Locate and identify every blood parasite.
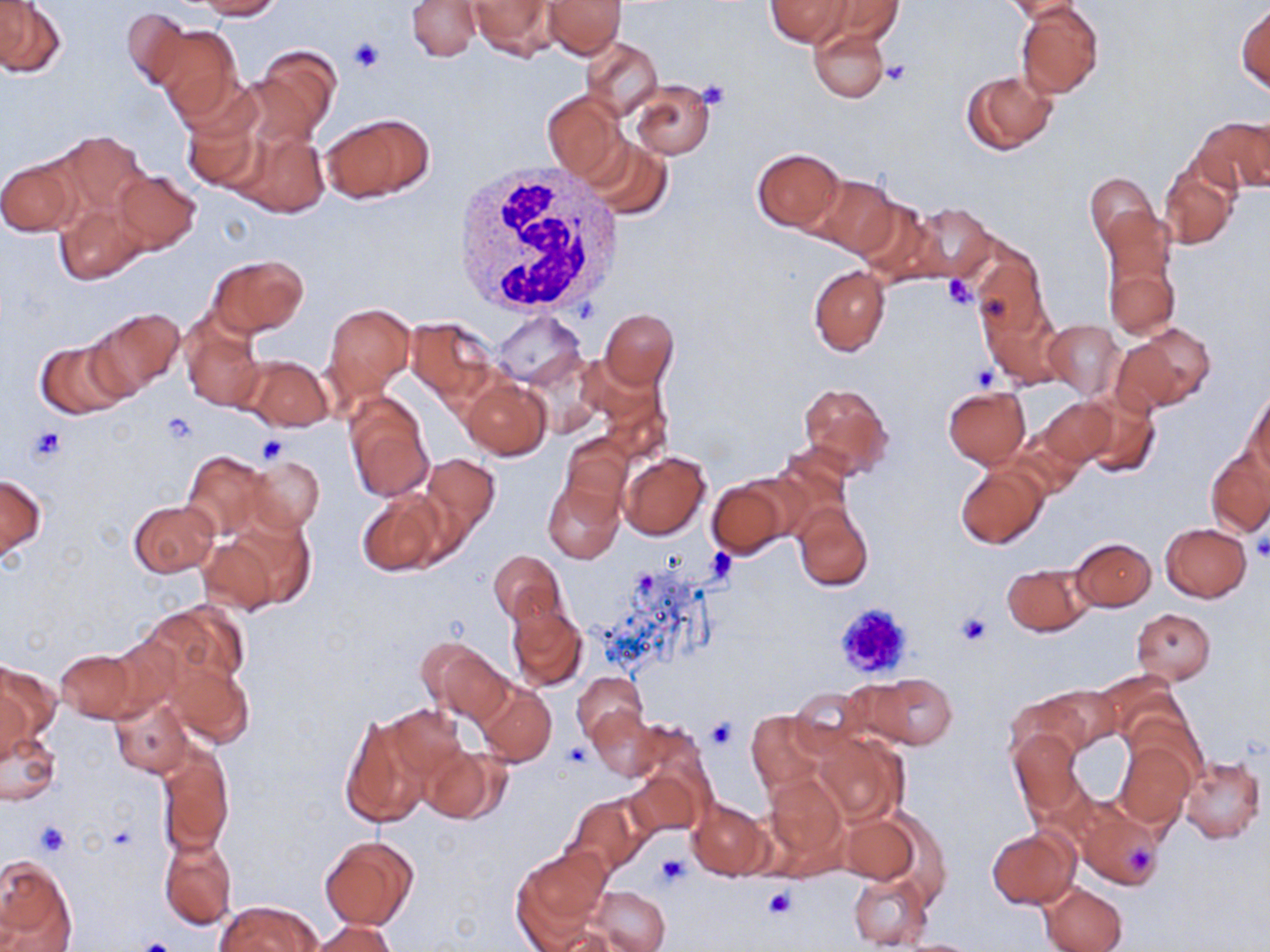
No blood parasites observed.

Summary:
  - Coordinate format: approximate bounding boxes as named x1/y1/x2/y2 corners in pixels
  - Platelet locations: (x1=348, y1=38, x2=383, y2=74), (x1=882, y1=61, x2=911, y2=86), (x1=695, y1=79, x2=731, y2=111), (x1=941, y1=277, x2=979, y2=311), (x1=973, y1=364, x2=1001, y2=390), (x1=160, y1=413, x2=198, y2=446), (x1=25, y1=425, x2=66, y2=464), (x1=258, y1=434, x2=290, y2=464), (x1=1251, y1=537, x2=1270, y2=563), (x1=831, y1=601, x2=915, y2=680), (x1=955, y1=613, x2=990, y2=647), (x1=705, y1=719, x2=737, y2=749), (x1=562, y1=743, x2=591, y2=770), (x1=35, y1=821, x2=68, y2=856), (x1=655, y1=852, x2=688, y2=886), (x1=763, y1=885, x2=797, y2=920), (x1=134, y1=936, x2=178, y2=952)
  - Uninfected red blood cell locations: (x1=198, y1=0, x2=280, y2=19), (x1=407, y1=0, x2=480, y2=61), (x1=543, y1=0, x2=624, y2=57), (x1=819, y1=0, x2=903, y2=45), (x1=466, y1=1, x2=559, y2=60), (x1=766, y1=1, x2=854, y2=47), (x1=1003, y1=1, x2=1084, y2=21), (x1=0, y1=2, x2=64, y2=76), (x1=1015, y1=2, x2=1104, y2=98), (x1=1237, y1=5, x2=1270, y2=94), (x1=122, y1=6, x2=189, y2=91), (x1=152, y1=23, x2=244, y2=122), (x1=809, y1=25, x2=891, y2=103), (x1=583, y1=38, x2=661, y2=117), (x1=250, y1=46, x2=342, y2=143), (x1=962, y1=70, x2=1056, y2=155), (x1=631, y1=81, x2=714, y2=159), (x1=542, y1=91, x2=625, y2=179), (x1=181, y1=107, x2=266, y2=193), (x1=320, y1=113, x2=436, y2=204), (x1=1194, y1=116, x2=1270, y2=195), (x1=233, y1=128, x2=330, y2=218), (x1=53, y1=130, x2=151, y2=221), (x1=583, y1=138, x2=673, y2=220), (x1=752, y1=148, x2=845, y2=232), (x1=0, y1=156, x2=79, y2=237), (x1=1158, y1=161, x2=1238, y2=248), (x1=112, y1=171, x2=201, y2=254), (x1=1085, y1=172, x2=1158, y2=252), (x1=804, y1=175, x2=900, y2=259), (x1=852, y1=199, x2=944, y2=285), (x1=55, y1=201, x2=149, y2=285), (x1=907, y1=203, x2=995, y2=283), (x1=1102, y1=229, x2=1179, y2=340), (x1=970, y1=247, x2=1047, y2=337), (x1=207, y1=253, x2=309, y2=337), (x1=808, y1=266, x2=890, y2=356), (x1=980, y1=301, x2=1065, y2=389), (x1=323, y1=302, x2=415, y2=401), (x1=83, y1=307, x2=185, y2=399), (x1=600, y1=309, x2=678, y2=389), (x1=490, y1=310, x2=588, y2=387), (x1=181, y1=315, x2=263, y2=412), (x1=404, y1=317, x2=500, y2=406), (x1=1043, y1=319, x2=1124, y2=401), (x1=1116, y1=323, x2=1210, y2=413), (x1=35, y1=340, x2=131, y2=421), (x1=239, y1=354, x2=332, y2=431), (x1=462, y1=378, x2=551, y2=460), (x1=797, y1=381, x2=893, y2=479), (x1=944, y1=386, x2=1030, y2=467), (x1=1244, y1=388, x2=1270, y2=480), (x1=344, y1=392, x2=433, y2=502), (x1=1075, y1=394, x2=1160, y2=478), (x1=1038, y1=399, x2=1115, y2=466), (x1=559, y1=433, x2=633, y2=515), (x1=1207, y1=449, x2=1270, y2=537), (x1=182, y1=450, x2=268, y2=540), (x1=619, y1=451, x2=710, y2=540), (x1=420, y1=454, x2=501, y2=542), (x1=248, y1=457, x2=324, y2=532), (x1=956, y1=465, x2=1048, y2=549), (x1=0, y1=474, x2=46, y2=559), (x1=541, y1=478, x2=625, y2=565), (x1=707, y1=479, x2=793, y2=557), (x1=355, y1=489, x2=447, y2=578), (x1=129, y1=500, x2=219, y2=577), (x1=793, y1=501, x2=873, y2=591), (x1=1160, y1=523, x2=1253, y2=602), (x1=196, y1=534, x2=283, y2=615), (x1=1071, y1=536, x2=1156, y2=610), (x1=488, y1=548, x2=566, y2=629), (x1=1002, y1=564, x2=1091, y2=637), (x1=147, y1=600, x2=251, y2=691), (x1=507, y1=600, x2=589, y2=692), (x1=1132, y1=608, x2=1216, y2=683), (x1=420, y1=637, x2=511, y2=725), (x1=56, y1=649, x2=139, y2=722), (x1=166, y1=661, x2=253, y2=746), (x1=0, y1=662, x2=59, y2=752), (x1=572, y1=672, x2=646, y2=742), (x1=863, y1=673, x2=957, y2=749), (x1=475, y1=681, x2=556, y2=766), (x1=1046, y1=684, x2=1123, y2=753), (x1=788, y1=688, x2=868, y2=755), (x1=1008, y1=694, x2=1088, y2=764), (x1=109, y1=695, x2=192, y2=778), (x1=383, y1=704, x2=468, y2=783), (x1=589, y1=707, x2=662, y2=780), (x1=747, y1=711, x2=826, y2=793), (x1=338, y1=714, x2=430, y2=828), (x1=628, y1=722, x2=711, y2=808), (x1=1, y1=725, x2=61, y2=807), (x1=1008, y1=729, x2=1086, y2=817), (x1=815, y1=732, x2=907, y2=826), (x1=1114, y1=740, x2=1194, y2=829), (x1=157, y1=743, x2=233, y2=855), (x1=420, y1=744, x2=509, y2=824), (x1=1177, y1=756, x2=1265, y2=843), (x1=623, y1=765, x2=706, y2=839), (x1=764, y1=773, x2=846, y2=871), (x1=567, y1=794, x2=650, y2=876), (x1=687, y1=796, x2=770, y2=881), (x1=1066, y1=796, x2=1166, y2=890), (x1=840, y1=814, x2=918, y2=884), (x1=988, y1=828, x2=1080, y2=909), (x1=159, y1=836, x2=237, y2=929), (x1=320, y1=836, x2=417, y2=929), (x1=514, y1=845, x2=611, y2=943), (x1=0, y1=854, x2=75, y2=951), (x1=846, y1=871, x2=933, y2=950), (x1=1040, y1=882, x2=1127, y2=952), (x1=588, y1=886, x2=672, y2=952), (x1=216, y1=900, x2=318, y2=952), (x1=311, y1=920, x2=397, y2=951), (x1=891, y1=938, x2=985, y2=951)
  - White blood cell locations: (x1=448, y1=163, x2=624, y2=320)
  - Slide-level diagnosis: negative for blood parasites
  - Preparation: thin blood smear
  - Modality: light microscopy
  - Stain: May-Grünwald-Giemsa
  - Magnification: 1000x
  - Image size: 1270×952 pixels
  - Field of view: one of a larger specimen